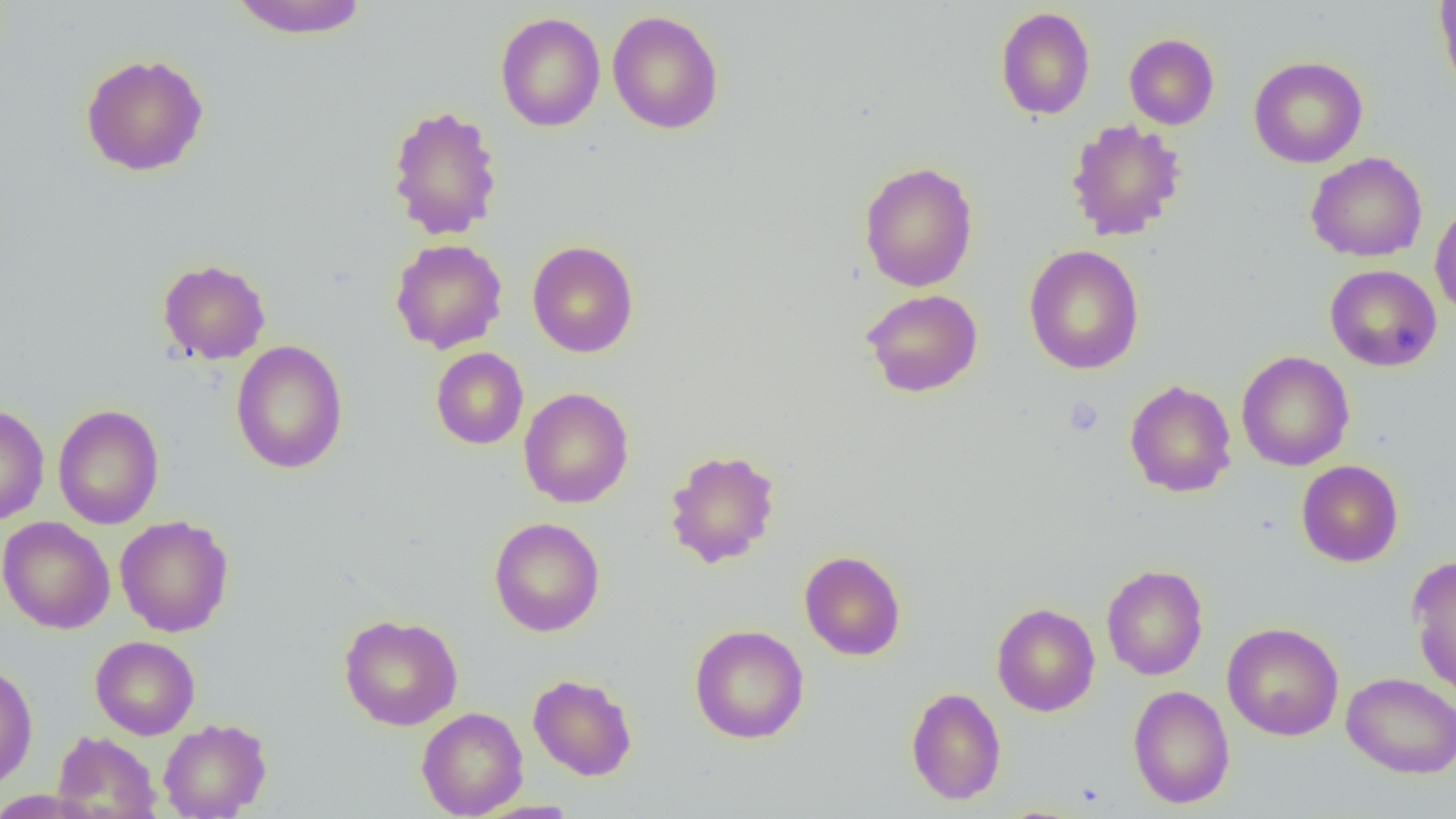

slide_level_diagnosis: negative for blood parasites
image_size: 1456×819 pixels
field_of_view: one of a larger specimen
modality: light microscopy
platelet_locations: 'approximate bounding boxes as (x1,y1)-(x2,y2) corner pairs in pixels: (1063,397)-(1104,437)'
preparation: thin blood film
magnification: 1000x
uninfected_red_blood_cell_locations: 'approximate bounding boxes as (x1,y1)-(x2,y2) corner pairs in pixels: (228,0)-(369,39), (1433,0)-(1456,100), (995,7)-(1095,120), (607,10)-(724,134), (495,12)-(605,132), (1124,33)-(1219,130), (80,53)-(209,177), (1249,56)-(1367,168), (386,103)-(504,241), (1066,119)-(1186,241), (1305,152)-(1428,262), (858,161)-(978,292), (1430,201)-(1456,320), (390,238)-(508,354), (527,240)-(639,358), (1023,245)-(1144,374), (157,259)-(271,365), (1324,264)-(1442,372), (860,288)-(983,397), (230,340)-(348,474), (430,347)-(529,449), (1236,350)-(1354,471), (1124,380)-(1237,497), (518,387)-(634,508), (0,404)-(49,526), (52,404)-(165,529), (663,448)-(782,569), (1296,460)-(1403,567), (114,515)-(234,637), (0,516)-(115,634), (488,517)-(605,637), (799,550)-(906,661), (1406,554)-(1456,699), (1102,564)-(1208,680), (991,602)-(1100,716), (338,613)-(463,730), (1222,622)-(1344,741), (689,624)-(809,743), (90,636)-(200,739), (0,661)-(38,791), (1342,672)-(1456,778), (528,673)-(638,781), (1128,685)-(1235,809), (905,687)-(1007,805), (416,707)-(528,818), (158,718)-(272,818), (52,731)-(162,819), (0,790)-(99,818)'